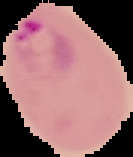
Malaria status: parasitized. Image is 133×157 pixels. From a thin blood smear. The area outside the segmented cell region is set to black.